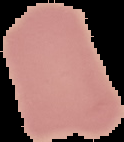
{
  "malaria_status": "uninfected",
  "image_type": "cell region segmented out of the field of view; surrounding area masked to black",
  "preparation": "thin blood film",
  "image_size": "124×142 pixels"
}